Report the malaria status of this cell.
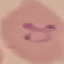
Parasitized.

Summary:
  - Image type: automatically extracted cell patch, resized to 64 × 64 pixels
  - Preparation: thin blood smear
  - Capture: smartphone camera at the microscope eyepiece
  - Stain: Giemsa